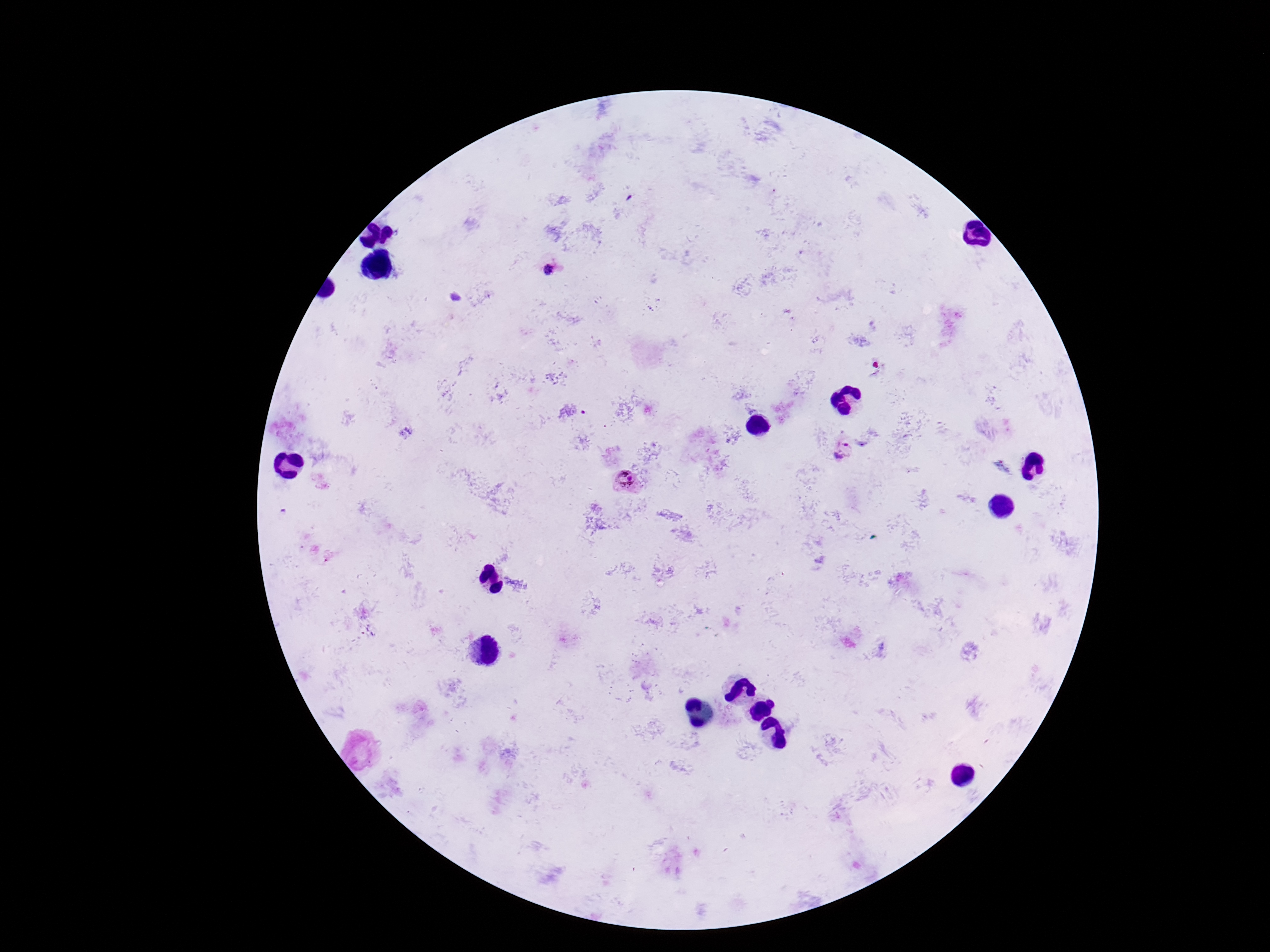

Approximate centers as (x, y) in pixels. Plasmodium parasite locations: (549, 271), (843, 450), (625, 480). Thick blood film. Image is 1270×952 pixels. 100x magnification. One field from this slide. Giemsa stain. Smartphone photograph taken through the microscope eyepiece. Patient malaria status: infected.